Point out each malaria parasite.
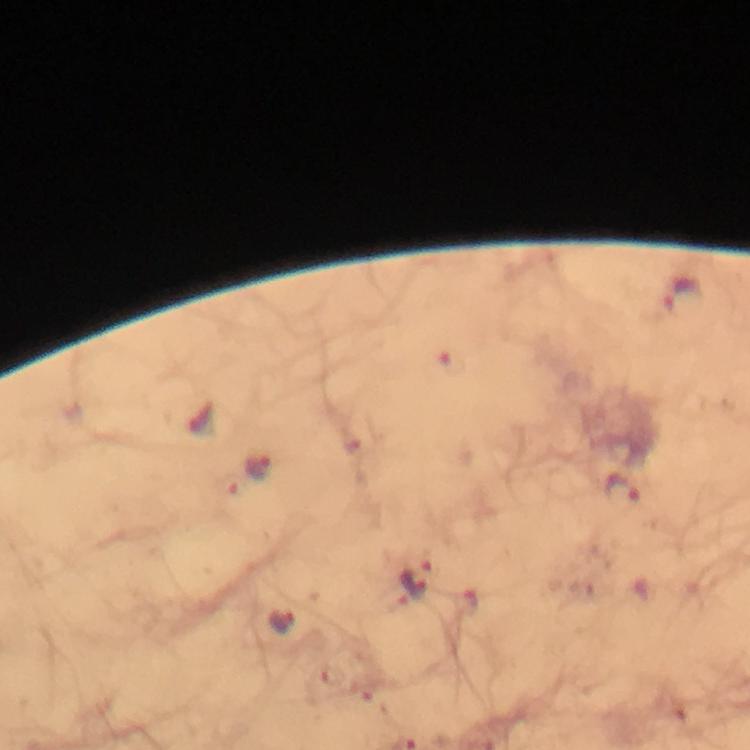
Approximate object centers, in pixels from the top-left corner.
Malaria parasites: (x=683, y=298), (x=453, y=362), (x=259, y=467), (x=621, y=492), (x=415, y=579), (x=464, y=601), (x=285, y=623).

{
  "magnification": "100x",
  "context": "from a malaria diagnostic workup",
  "immersion_oil": "applied",
  "capture": "smartphone photograph through a microscope",
  "stain": "Giemsa",
  "image_size": "750×750 pixels",
  "preparation": "thick smear",
  "cropped_from": "one field of view"
}